Name the parasite shown.
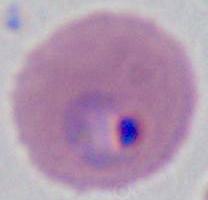

This is Plasmodium.

modality = photomicrograph
magnification = 400x or 1000x